Report the malaria status of this cell.
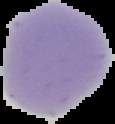

Uninfected.

Segmented cell region on a black background. From a thin blood smear. Image is 115×124 pixels.